State the blood parasite species.
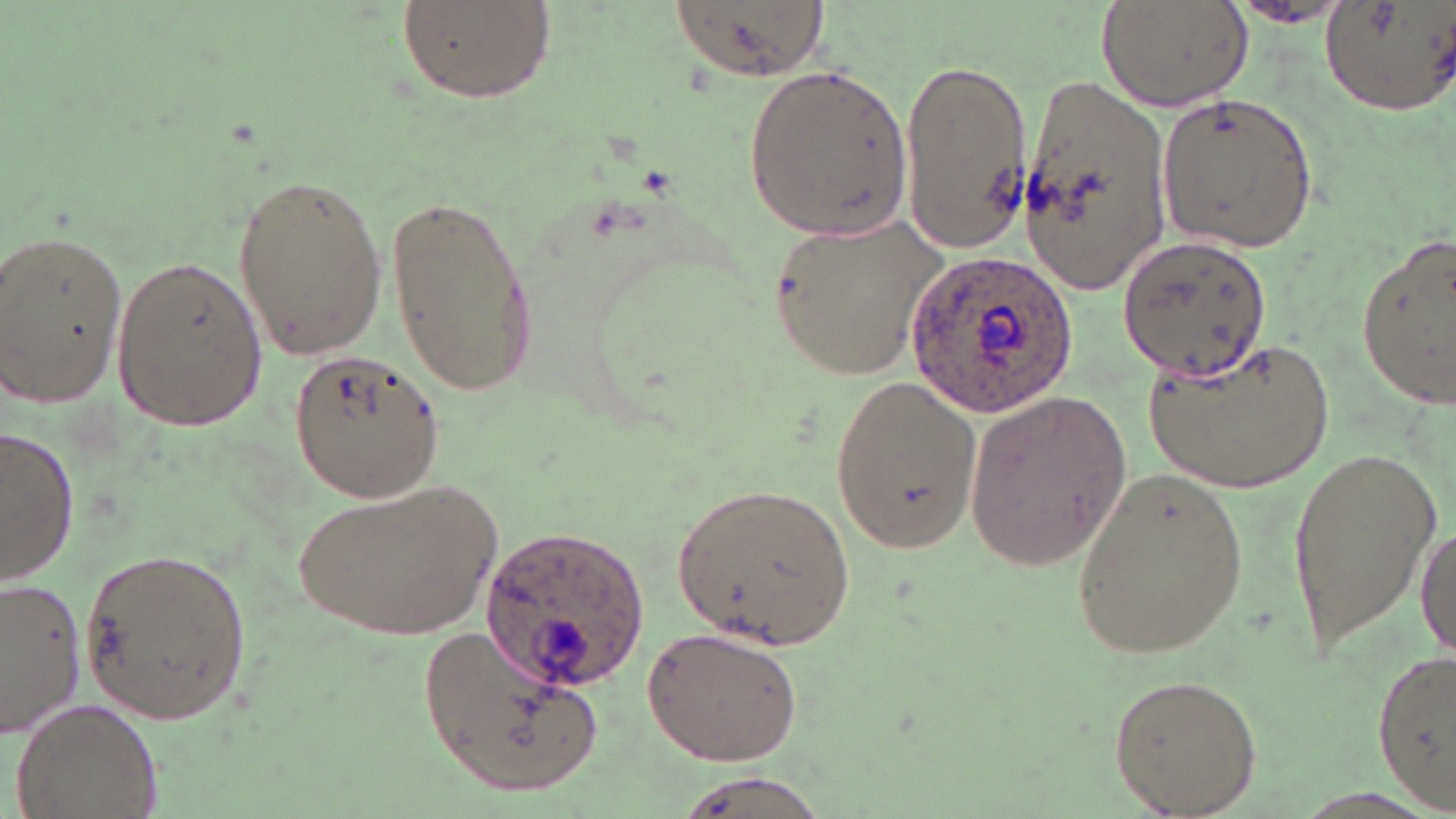
Plasmodium ovale.

uninfected red blood cell locations = approximate bounding boxes as (x1, y1, x2, y2) in pixels: (390, 0, 558, 105), (661, 0, 836, 79), (1096, 0, 1249, 113), (1319, 1, 1455, 115), (1221, 3, 1354, 28), (896, 54, 1033, 254), (741, 64, 920, 239), (1021, 68, 1174, 293), (1155, 91, 1320, 255), (229, 169, 388, 363), (387, 191, 542, 395), (766, 217, 950, 377), (1, 227, 131, 408), (1354, 229, 1456, 412), (1115, 234, 1272, 381), (110, 251, 267, 433), (1147, 334, 1336, 492), (289, 349, 447, 506), (828, 376, 982, 558), (963, 389, 1131, 573), (1, 426, 77, 588), (1281, 442, 1438, 653), (1068, 467, 1251, 665), (287, 475, 505, 644), (666, 480, 854, 652), (1415, 523, 1455, 664), (78, 543, 253, 726), (0, 574, 88, 739), (420, 620, 600, 798), (641, 625, 806, 766), (1374, 648, 1453, 808), (1106, 671, 1263, 816), (12, 694, 164, 819), (663, 772, 837, 819)
preparation = thin blood film
Plasmodium ovale-infected red blood cell locations = approximate bounding boxes as (x1, y1, x2, y2) in pixels: (907, 247, 1076, 421), (481, 522, 649, 691)
stain = May-Grünwald-Giemsa
image size = 1456×819 pixels
magnification = 1000x
field of view = single
modality = optical microscopy